Describe the morphology of the red blood cells.
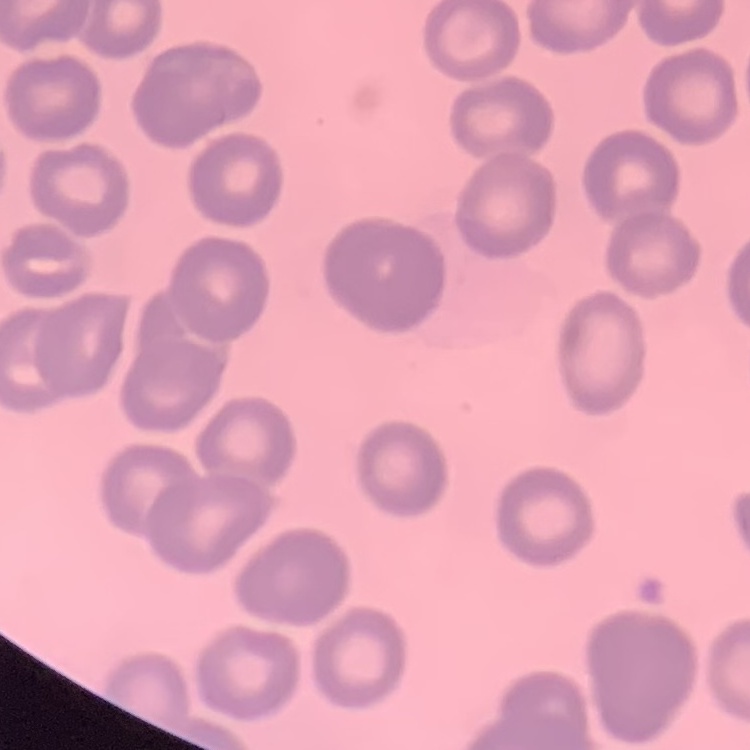
No rouleaux formation.

Summary:
  - Image type: one tile cut from a larger photomicrograph
  - Stain: Field's or Giemsa
  - Preparation: thin blood film